State which parasite is depicted.
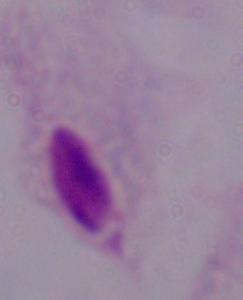

A trichomonad.

Micrograph. Captured at 1000x magnification.